State which cell type is depicted.
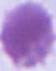

This is an erythrocyte.

Captured at 1000x magnification. Micrograph.